Identify the cell.
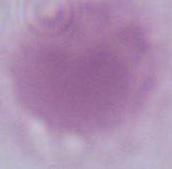

This is an erythrocyte.

Summary:
  - Modality: photomicrograph
  - Magnification: 1000x